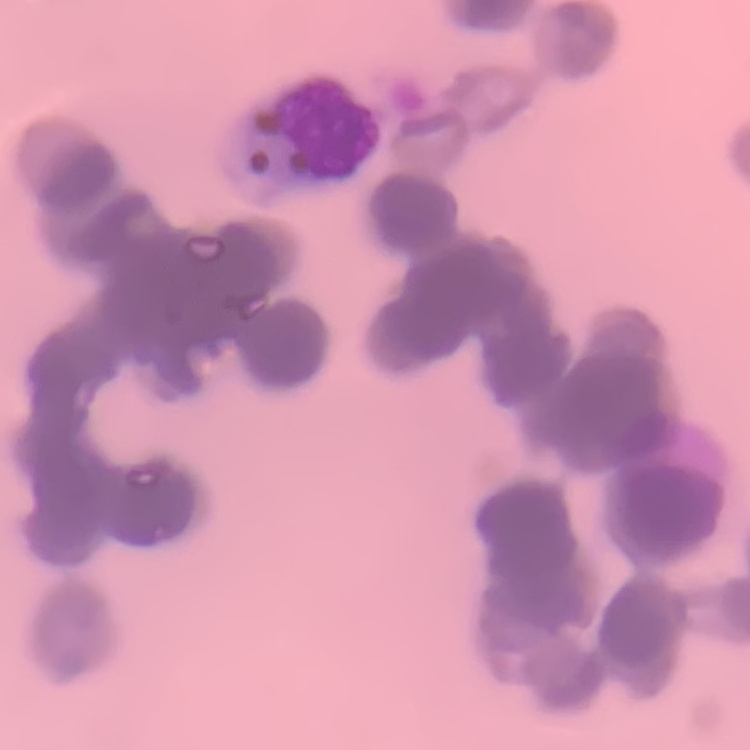 The red blood cells exhibit rouleaux formation. One tile cut from a larger photomicrograph. Thin blood film. Stained with either Field's or Giemsa.